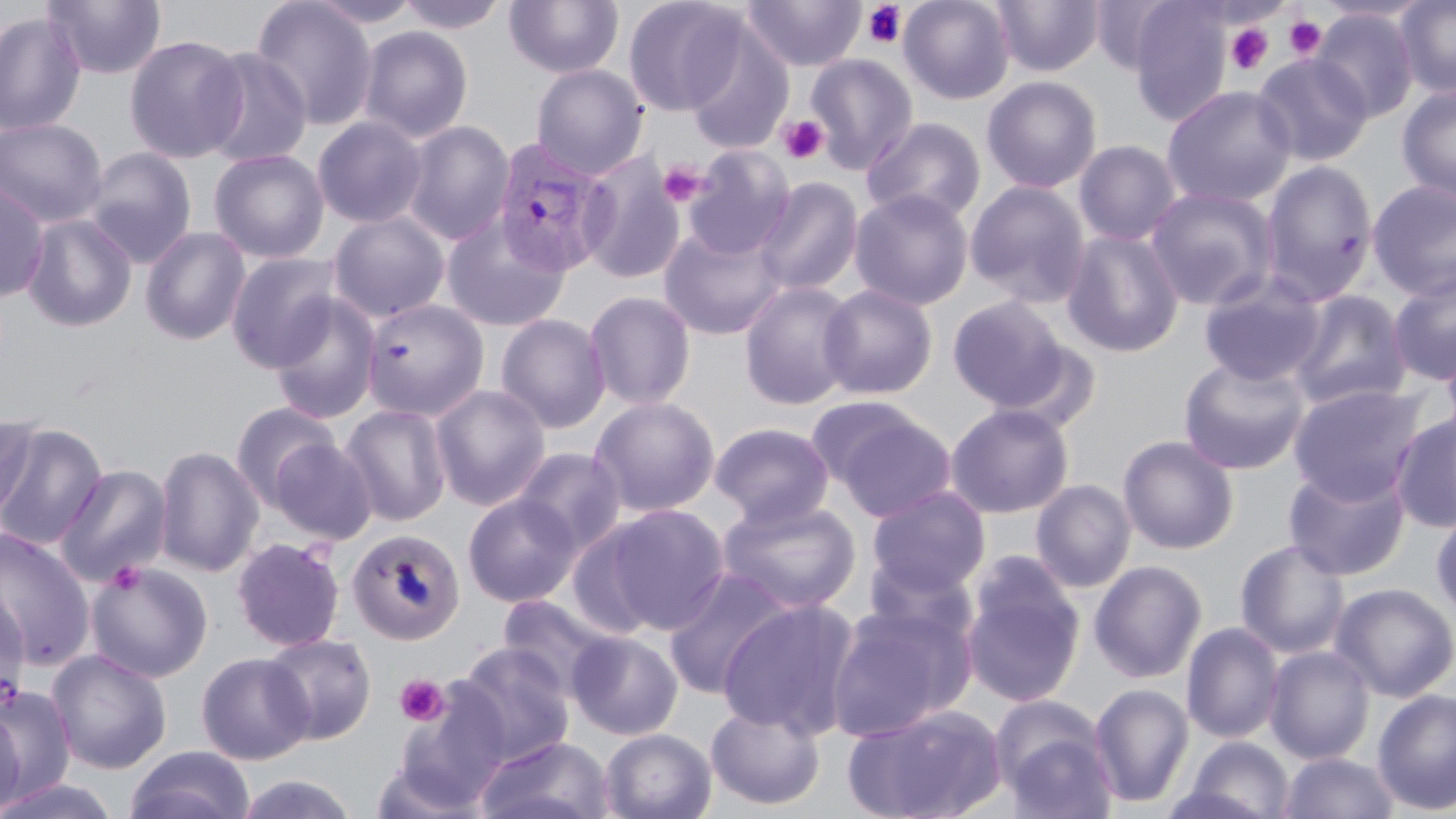

Summary:
  - Coordinate format: approximate bounding boxes as [x1, y1, x2, y2] in pixels
  - Uninfected red blood cell locations: [42, 0, 166, 81], [250, 0, 378, 131], [305, 0, 425, 28], [395, 0, 510, 34], [623, 0, 747, 116], [741, 0, 866, 72], [898, 0, 1015, 105], [991, 0, 1103, 77], [1396, 0, 1456, 100], [504, 1, 624, 78], [1088, 1, 1179, 77], [1126, 2, 1233, 125], [1312, 8, 1419, 123], [0, 10, 86, 137], [357, 26, 474, 143], [683, 28, 794, 154], [123, 33, 248, 163], [197, 47, 314, 168], [1252, 52, 1374, 166], [805, 53, 918, 175], [531, 64, 648, 179], [981, 76, 1102, 194], [1161, 85, 1297, 209], [1396, 85, 1456, 206], [312, 116, 429, 229], [0, 117, 108, 227], [862, 117, 986, 226], [401, 121, 515, 245], [1073, 140, 1183, 247], [682, 145, 795, 260], [81, 147, 198, 268], [208, 149, 329, 263], [579, 153, 686, 284], [1259, 159, 1379, 305], [753, 176, 863, 297], [1366, 179, 1456, 300], [965, 180, 1090, 308], [0, 181, 50, 302], [1144, 186, 1279, 310], [850, 188, 974, 311], [327, 211, 451, 323], [21, 214, 137, 332], [441, 215, 571, 331], [657, 224, 786, 341], [140, 226, 251, 345], [1060, 229, 1185, 358], [225, 252, 342, 372], [1388, 269, 1456, 386], [1197, 272, 1326, 386], [738, 281, 860, 411], [818, 284, 939, 400], [1287, 290, 1411, 410], [584, 291, 696, 410], [267, 293, 382, 425], [946, 296, 1072, 411], [360, 298, 489, 421], [495, 313, 611, 434], [1440, 343, 1456, 452], [1178, 355, 1311, 475], [1288, 382, 1427, 505], [430, 383, 551, 511], [589, 396, 721, 518], [230, 402, 340, 510], [340, 403, 452, 527], [945, 403, 1074, 519], [821, 406, 956, 522], [1390, 410, 1456, 533], [0, 412, 39, 525], [709, 422, 835, 527], [0, 423, 108, 551], [1117, 435, 1239, 554], [268, 437, 377, 544], [153, 445, 265, 578], [512, 446, 626, 556], [54, 463, 173, 587], [1283, 465, 1411, 581], [1030, 479, 1136, 594], [866, 486, 991, 598], [463, 493, 581, 608], [717, 497, 862, 615], [600, 504, 730, 634], [1431, 506, 1456, 625], [565, 522, 662, 640], [0, 528, 95, 670], [346, 529, 465, 646], [231, 537, 346, 652], [1234, 539, 1352, 658], [859, 554, 982, 659], [960, 558, 1086, 710], [86, 560, 213, 683], [1088, 560, 1208, 683], [662, 567, 797, 699], [1329, 582, 1456, 702], [0, 588, 31, 704], [496, 594, 619, 700], [715, 599, 860, 740], [823, 599, 973, 743], [1181, 622, 1283, 744], [567, 630, 683, 741], [262, 632, 377, 745], [454, 643, 574, 766], [1263, 645, 1375, 763], [46, 648, 172, 774], [196, 652, 314, 764], [1089, 682, 1194, 808], [392, 684, 512, 810], [1, 685, 76, 800], [1372, 688, 1456, 815], [992, 698, 1118, 818], [705, 702, 825, 811], [842, 704, 1008, 819], [0, 706, 25, 818], [599, 728, 717, 819], [474, 736, 615, 819], [1177, 736, 1296, 819], [124, 745, 255, 819], [1279, 751, 1397, 818], [232, 774, 359, 819], [0, 776, 121, 819]
  - Plasmodium vivax-infected red blood cell locations: [491, 139, 613, 279]
  - Platelet locations: [862, 2, 908, 49], [1284, 15, 1327, 59], [1225, 22, 1274, 76], [778, 115, 828, 164], [656, 160, 706, 209], [395, 674, 449, 727]
  - Slide-level diagnosis: Plasmodium vivax
  - Image size: 1456×819 pixels
  - Stain: May-Grünwald-Giemsa
  - Magnification: 1000x
  - Preparation: thin blood film
  - Field of view: single
  - Modality: light microscopy